Outline each Babesia divergens-infected red blood cell.
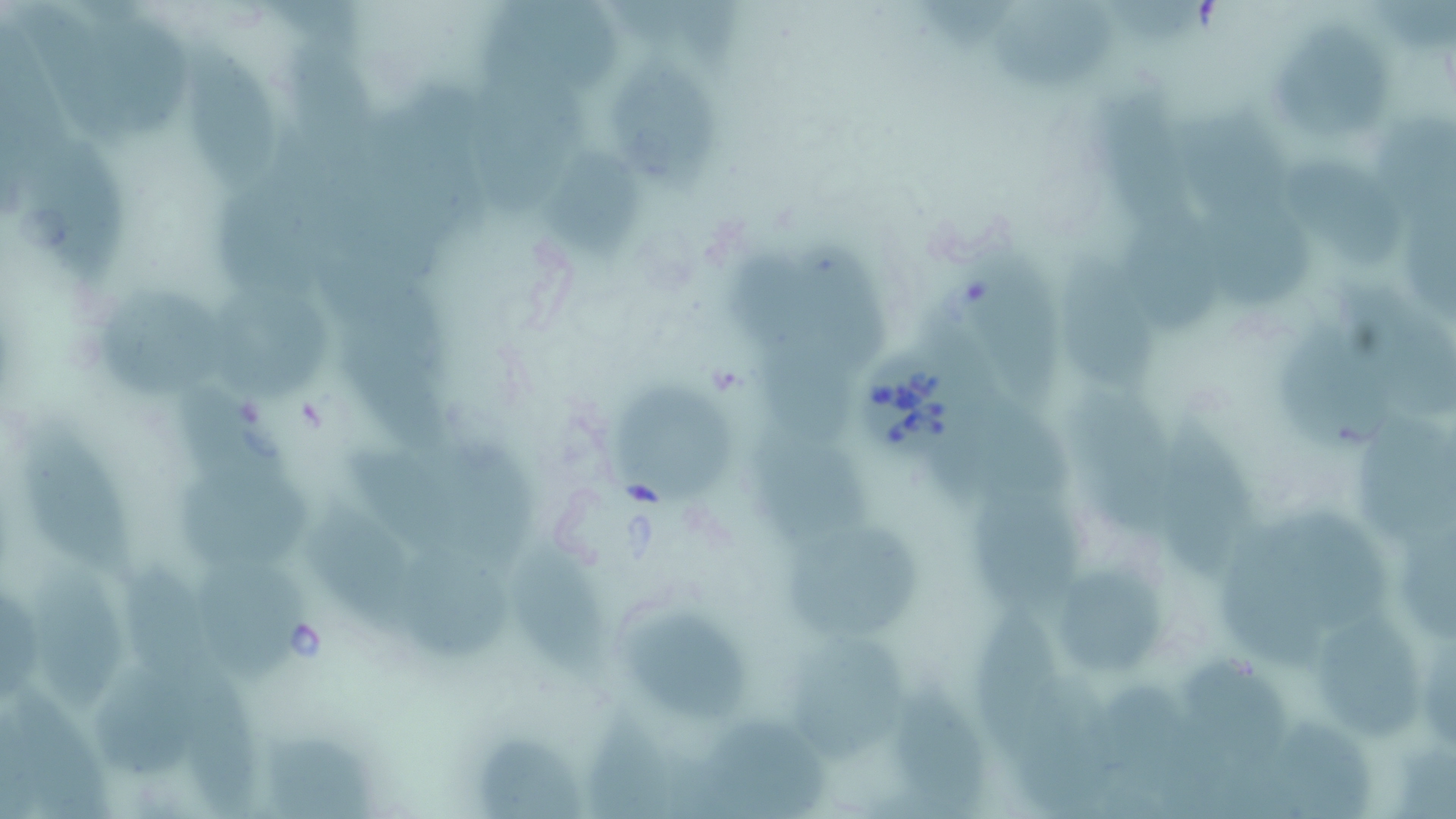

Approximate bounding boxes as [x1, y1, x2, y2] in pixels.
Babesia divergens-infected red blood cells: [859, 344, 979, 456].

Uninfected red blood cell locations: [481, 0, 631, 96], [933, 0, 1032, 62], [993, 0, 1127, 96], [1121, 0, 1209, 46], [23, 9, 126, 145], [106, 29, 197, 139], [1288, 30, 1398, 148], [287, 38, 377, 175], [173, 49, 286, 184], [631, 68, 727, 198], [476, 69, 599, 222], [1111, 85, 1207, 230], [1381, 104, 1456, 204], [1197, 117, 1308, 222], [27, 147, 129, 296], [552, 153, 646, 266], [1302, 165, 1398, 269], [217, 203, 314, 312], [1223, 214, 1319, 309], [1130, 220, 1220, 340], [804, 234, 898, 361], [964, 244, 1081, 400], [728, 250, 830, 352], [318, 251, 453, 380], [1060, 253, 1164, 396], [1325, 275, 1456, 415], [220, 295, 335, 401], [113, 303, 237, 397], [1284, 329, 1406, 450], [757, 340, 866, 455], [350, 348, 453, 464], [1062, 375, 1169, 529], [613, 376, 737, 506], [198, 388, 306, 505], [1154, 401, 1253, 570], [945, 403, 1077, 509], [1363, 411, 1456, 529], [24, 415, 139, 592], [752, 430, 877, 544], [453, 447, 554, 552], [344, 450, 469, 560], [188, 480, 328, 576], [981, 494, 1085, 613], [1244, 501, 1373, 615], [1400, 510, 1456, 631], [307, 514, 418, 627], [790, 522, 929, 637], [412, 536, 511, 660], [1227, 547, 1329, 667], [528, 557, 613, 680], [122, 562, 222, 694], [42, 566, 134, 711], [209, 569, 304, 687], [1072, 570, 1166, 682], [4, 573, 43, 706], [623, 605, 763, 723], [977, 605, 1047, 759], [1319, 608, 1420, 734], [791, 632, 906, 747], [1417, 632, 1456, 739], [1189, 654, 1282, 763], [1026, 672, 1119, 814], [883, 675, 984, 819], [1110, 676, 1208, 819], [184, 682, 264, 819], [19, 686, 107, 817], [106, 690, 205, 773], [598, 711, 689, 816], [1280, 717, 1374, 813], [713, 718, 828, 812], [484, 727, 579, 817], [259, 731, 383, 818], [1390, 741, 1456, 819]. Slide-level diagnosis: Babesia divergens. Captured at 1000x magnification. May-Grünwald-Giemsa stain. Single field of view. Light microscopy. Image is 1456×819 pixels. Thin blood smear.